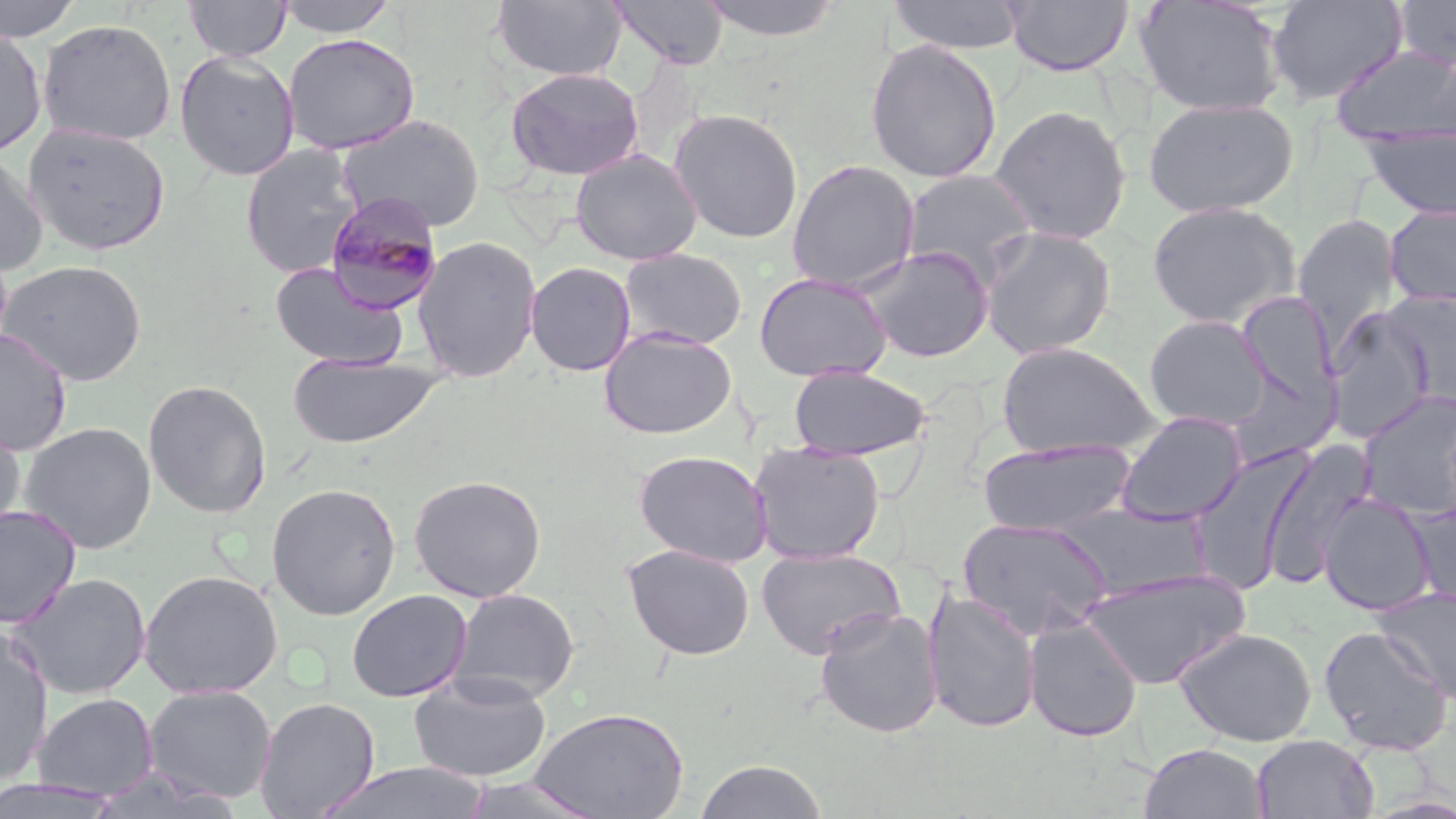
Summary:
  - Coordinate format: approximate bounding boxes as (x1,y1)-(x2,y2) corner pairs in pixels
  - Plasmodium malariae-infected red blood cell locations: (323,191)-(444,316)
  - Uninfected red blood cell locations: (0,0)-(84,41), (184,0)-(291,61), (274,0)-(401,38), (491,0)-(627,83), (610,0)-(730,70), (697,0)-(846,42), (887,0)-(1026,55), (1004,0)-(1133,76), (1134,0)-(1286,118), (1266,0)-(1408,105), (1391,0)-(1456,70), (37,19)-(176,146), (0,26)-(48,158), (283,33)-(420,155), (864,39)-(1003,184), (1332,45)-(1456,147), (174,49)-(300,181), (505,66)-(645,181), (1142,97)-(1299,218), (989,104)-(1131,244), (668,107)-(804,244), (337,114)-(486,232), (23,121)-(172,256), (1360,124)-(1456,222), (240,143)-(366,279), (0,148)-(48,275), (569,149)-(703,266), (785,159)-(920,291), (900,168)-(1040,285), (1147,201)-(1301,327), (1384,204)-(1456,308), (1293,215)-(1403,351), (979,225)-(1116,360), (412,235)-(542,383), (858,245)-(994,362), (619,248)-(748,350), (0,260)-(148,386), (269,261)-(408,371), (525,261)-(636,376), (753,271)-(891,382), (1381,290)-(1456,408), (1236,291)-(1338,405), (1325,309)-(1435,437), (1144,314)-(1271,430), (600,327)-(737,439), (0,328)-(73,456), (996,341)-(1160,458), (286,352)-(444,449), (1224,364)-(1339,470), (787,365)-(931,460), (142,378)-(272,519), (1358,391)-(1456,520), (1116,411)-(1248,525), (0,418)-(26,539), (18,421)-(158,554), (977,439)-(1135,536), (749,442)-(886,565), (1259,444)-(1373,588), (633,449)-(773,567), (1187,449)-(1312,594), (408,474)-(547,602), (265,482)-(402,620), (1318,493)-(1437,615), (1407,501)-(1456,607), (0,504)-(82,630), (957,517)-(1112,639), (622,544)-(756,661), (755,546)-(906,659), (139,568)-(284,699), (1078,568)-(1250,690), (6,572)-(152,700), (448,587)-(580,703), (1373,587)-(1456,702), (923,588)-(1041,734), (347,589)-(472,703), (814,607)-(944,738), (1023,616)-(1142,742), (1318,625)-(1453,755), (0,626)-(54,788), (1173,626)-(1318,747), (408,671)-(553,782), (144,684)-(277,805), (32,693)-(159,800), (254,697)-(381,818), (530,706)-(689,819), (1251,734)-(1378,819), (1139,742)-(1268,819), (694,759)-(828,819), (318,762)-(491,819), (454,775)-(607,819), (0,776)-(126,818)
  - Slide-level diagnosis: Plasmodium malariae
  - Modality: light microscopy
  - Stain: May-Grünwald-Giemsa
  - Field of view: one of a larger specimen
  - Preparation: thin blood film
  - Image size: 1456×819 pixels
  - Magnification: 1000x